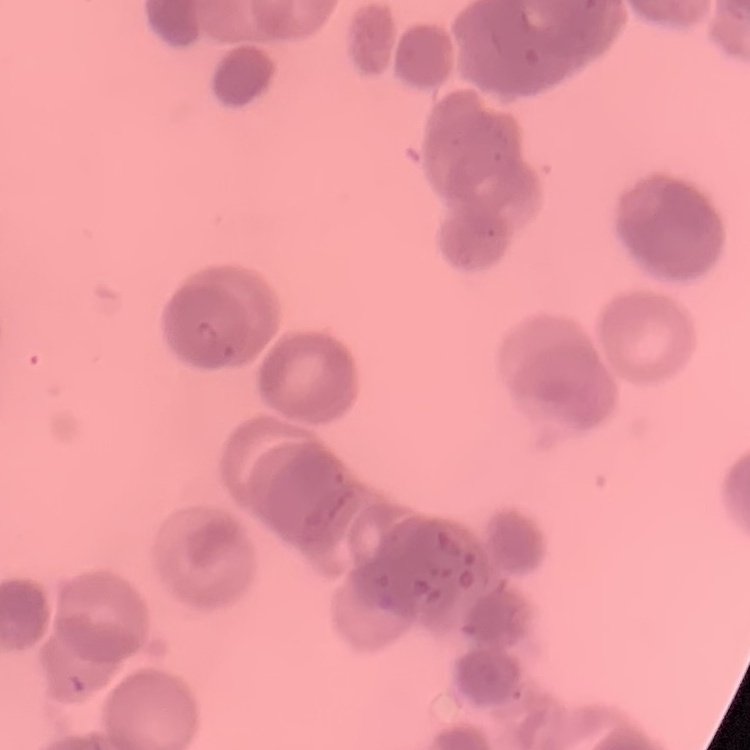

Summary:
  - Erythrocyte morphology: rouleaux formation
  - Stain: Field's or Giemsa
  - Preparation: thin blood smear
  - Image type: square crop of a larger photomicrograph